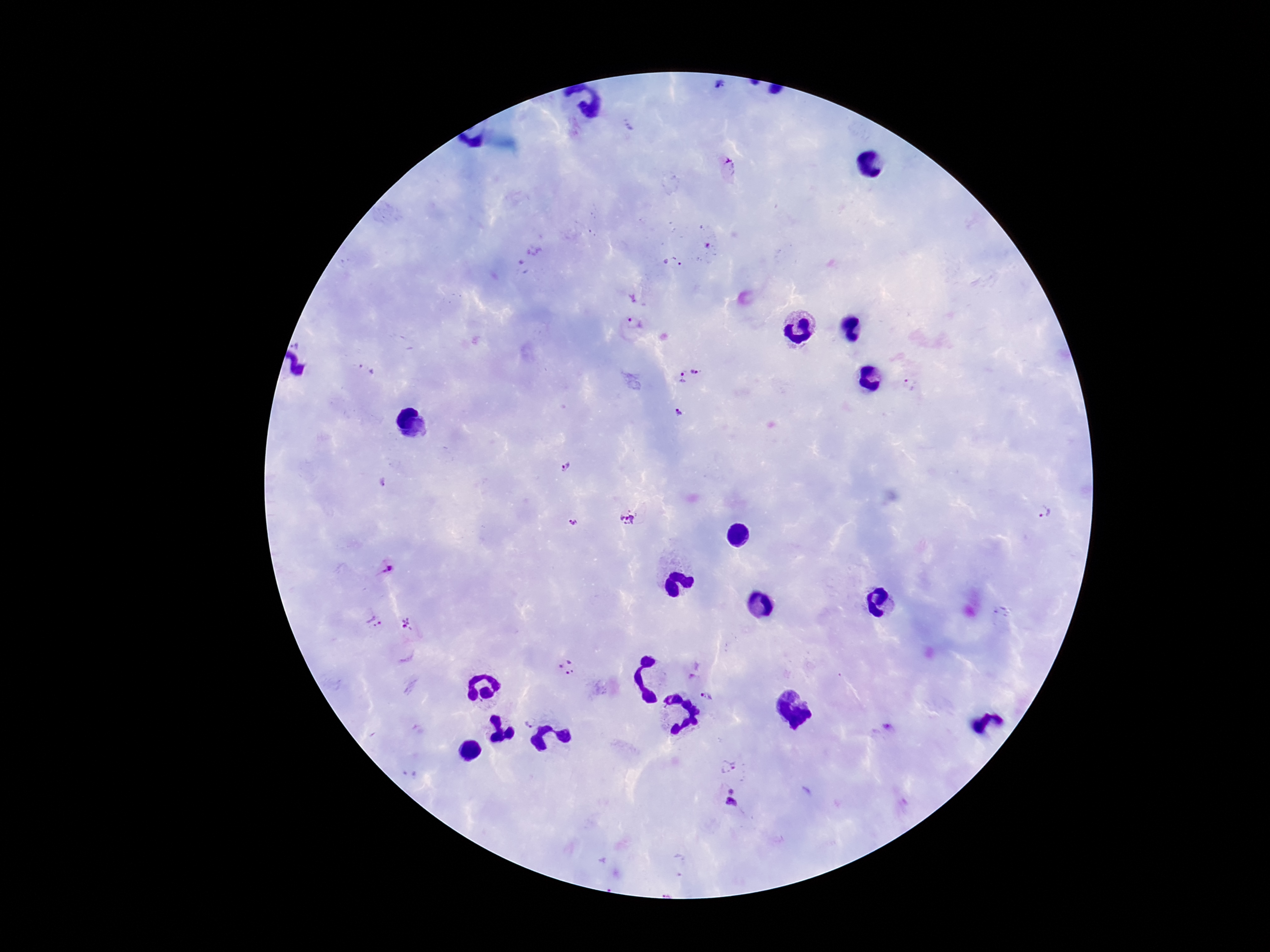
Approximate centers as [x, y] in pixels. Plasmodium parasite locations: [719, 89], [730, 170], [707, 245], [528, 258], [671, 262], [635, 323], [695, 369], [366, 370], [680, 379], [909, 385], [679, 412], [565, 468], [382, 481], [1041, 514], [628, 518], [572, 521], [387, 570], [374, 621], [408, 625], [566, 667], [707, 697], [530, 722], [889, 728], [729, 766], [731, 790], [731, 806]. One field from this slide. Giemsa stain. Smartphone photograph taken through the microscope eyepiece. Image is 1270×952 pixels. 100x magnification. Patient malaria status: positive. Thick peripheral-blood smear.